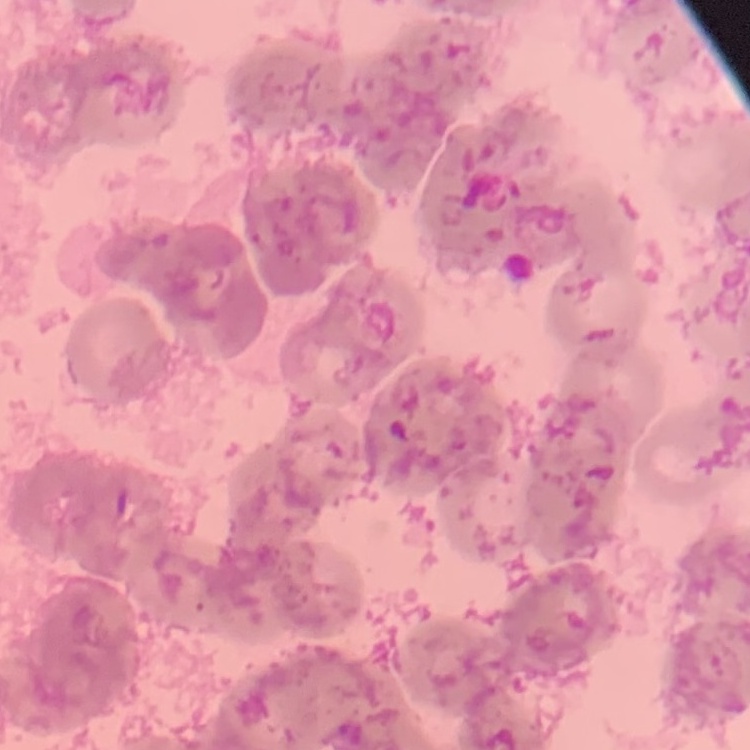
The erythrocytes exhibit rouleaux formation. Field's or Giemsa stain. Thin blood film. One tile cut from a larger photomicrograph.